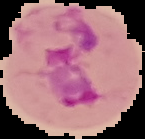

Summary:
  - Image size: 145×139 pixels
  - Image type: cell region segmented out of the field of view; surrounding area masked to black
  - Preparation: thin blood smear
  - Malaria status: parasitized